Identify the parasite.
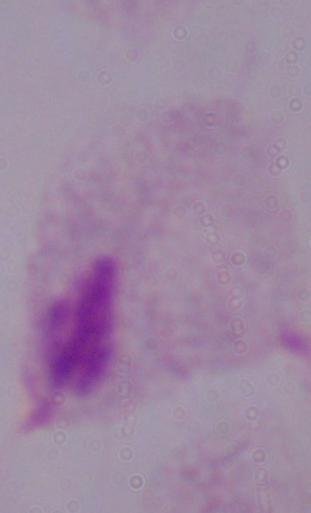

This is a trichomonad.

Captured at 1000x magnification. Micrograph.